Point out every Plasmodium parasite.
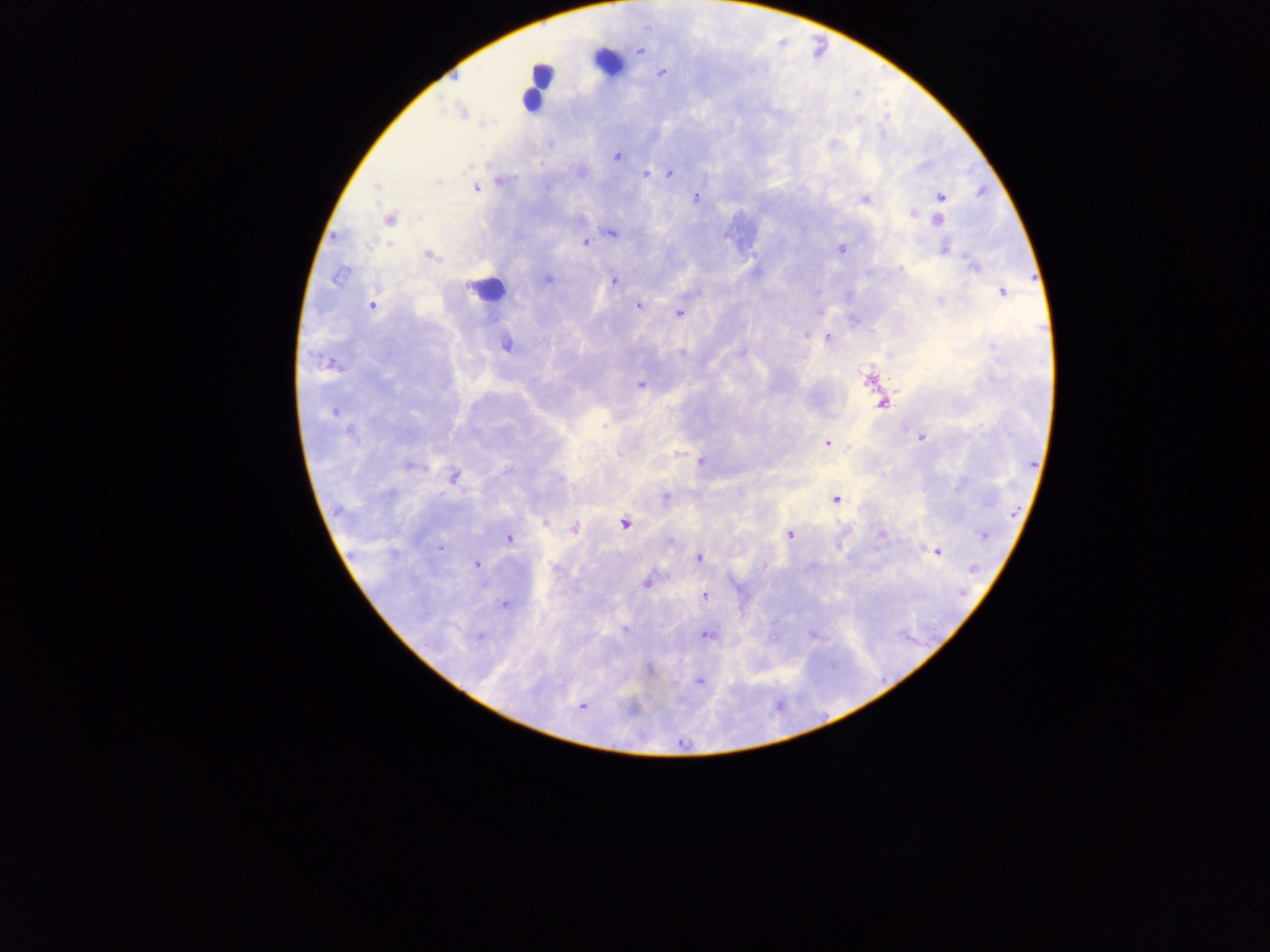

Approximate centers as {x, y} in pixels.
Plasmodium parasites: {640, 51}, {663, 72}, {462, 113}, {550, 145}, {617, 156}, {669, 173}, {647, 174}, {501, 181}, {375, 188}, {476, 188}, {982, 191}, {696, 197}, {940, 197}, {865, 199}, {913, 214}, {389, 219}, {938, 220}, {612, 232}, {335, 237}, {585, 242}, {841, 249}, {945, 250}, {429, 255}, {973, 265}, {901, 269}, {337, 277}, {547, 279}, {613, 281}, {1004, 291}, {939, 301}, {372, 305}, {639, 305}, {822, 313}, {679, 314}, {806, 335}, {828, 337}, {506, 345}, {741, 353}, {868, 379}, {640, 384}, {882, 404}, {334, 412}, {349, 432}, {921, 437}, {827, 444}, {701, 462}, {408, 466}, {507, 470}, {454, 477}, {559, 479}, {391, 493}, {666, 498}, {836, 499}, {338, 510}, {545, 523}, {624, 524}, {574, 528}, {882, 534}, {790, 535}, {983, 535}, {509, 538}, {670, 541}, {440, 548}, {938, 551}, {699, 557}, {477, 564}, {975, 568}, {646, 584}, {705, 596}, {505, 605}, {623, 629}, {707, 634}, {478, 636}, {650, 668}, {699, 681}, {582, 706}, {631, 709}.

Summary:
  - Leukocyte locations (subset; some below the resolvable size): {608, 61}, {539, 83}, {532, 96}, {740, 234}, {487, 289}
  - Field of view: single
  - Image size: 1270×952 pixels
  - Preparation: thick blood film
  - Country: Ghana
  - Capture: mobile-phone photograph through a microscope